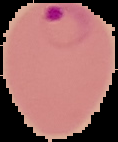 Image is 118×142 pixels. From a thin blood film. The area outside the segmented cell region is set to black. Malaria status: parasitized.